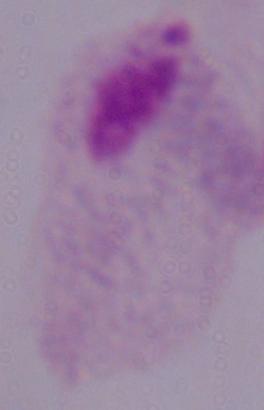 A trichomonad is seen. Micrograph. 1000x magnification.